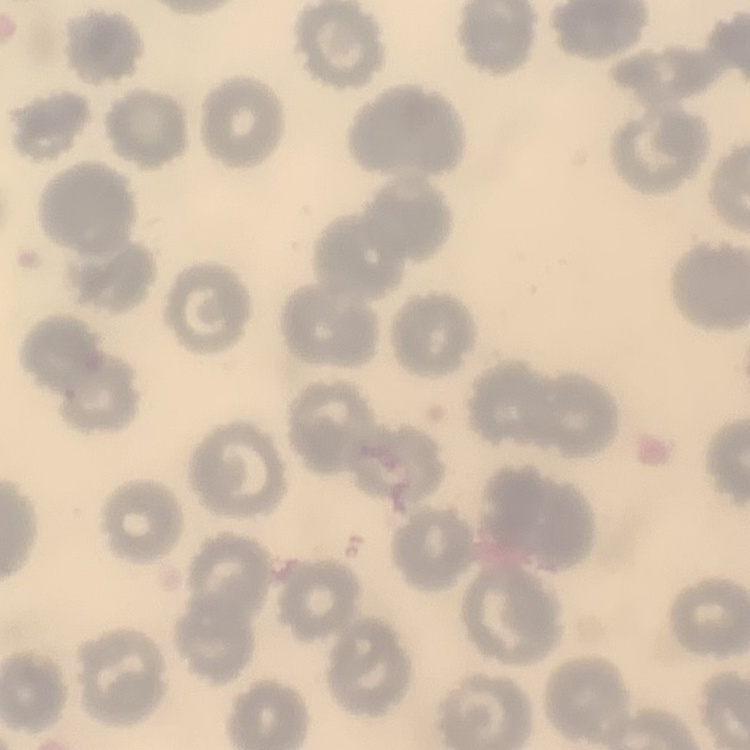

erythrocyte_morphology: no rouleaux formation
preparation: thin blood smear
stain: Field's or Giemsa
image_type: one tile cut from a larger photomicrograph